Comment on the morphology of the red blood cells.
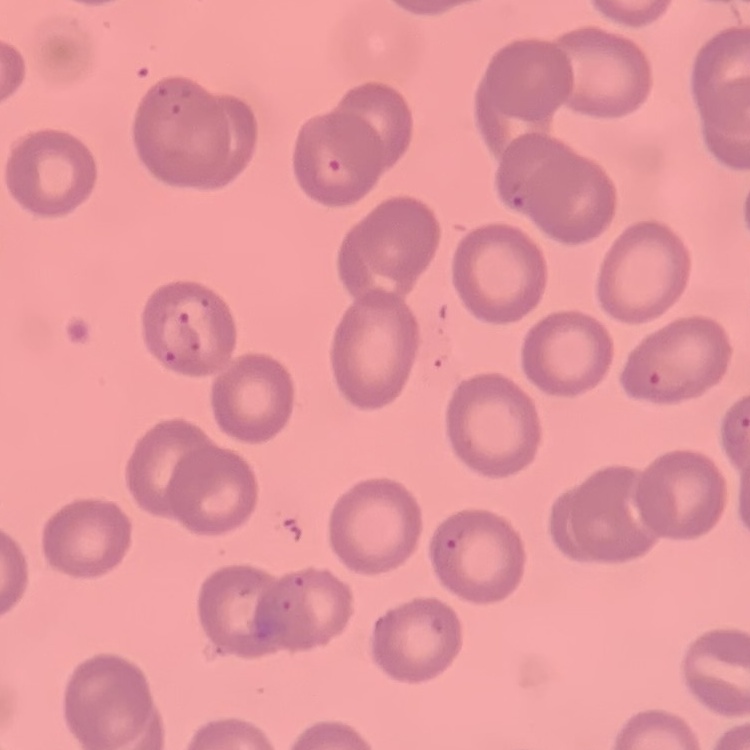
They show no rouleaux formation.

Thin blood film. Field's or Giemsa stain. One tile cut from a larger photomicrograph.